Assess this cell for malaria.
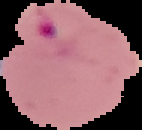

Parasitized.

Summary:
  - Image size: 142×130 pixels
  - Preparation: thin blood film
  - Image type: cell region segmented out of the field of view; surrounding area masked to black